State the blood parasite species.
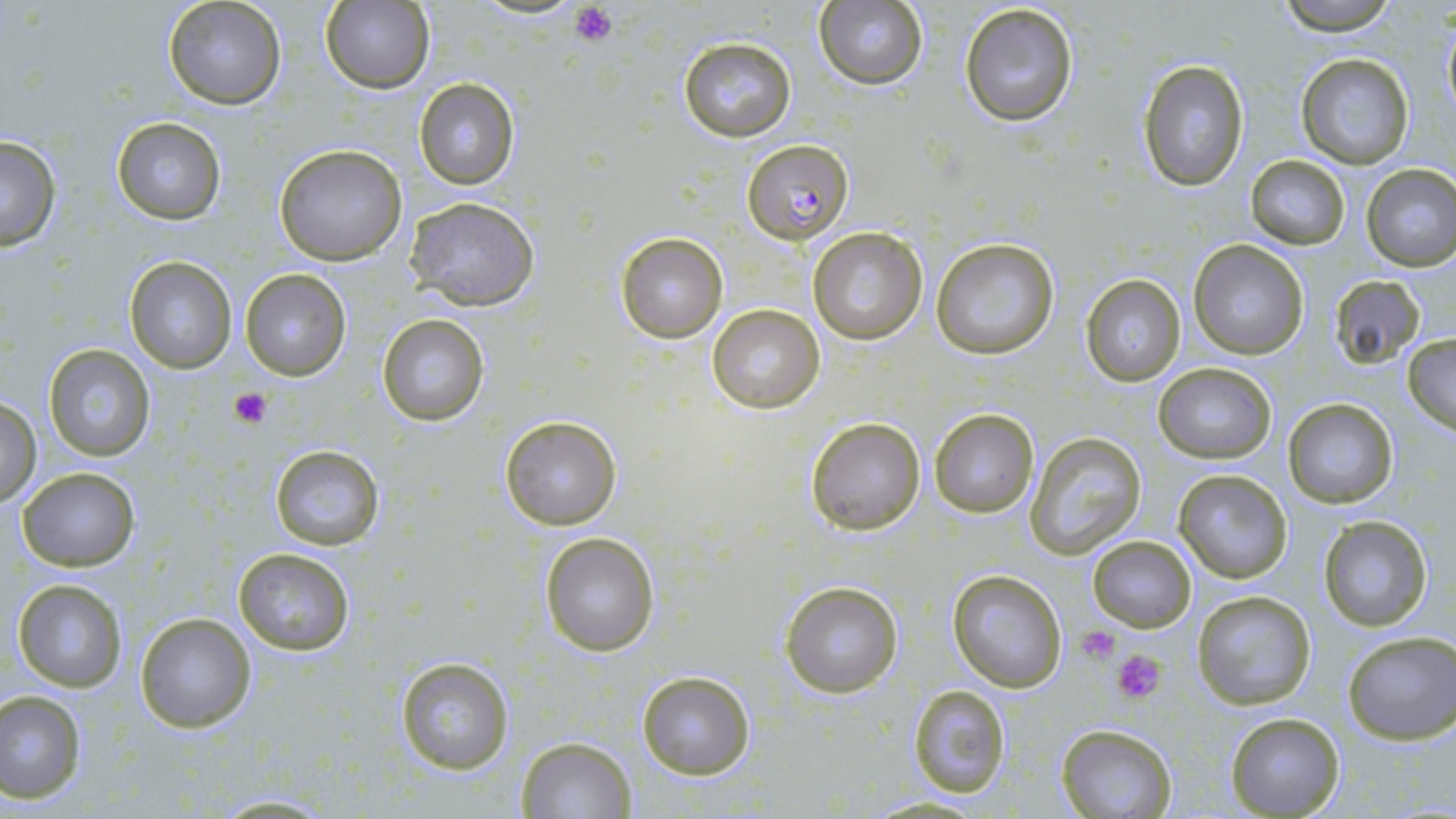

Plasmodium falciparum.

Summary:
  - Coordinate format: approximate bounding boxes as (x1, y1, x2, y2) in pixels
  - Plasmodium falciparum-infected red blood cell locations: (742, 140, 852, 242)
  - Uninfected red blood cell locations: (161, 0, 287, 111), (1273, 0, 1401, 33), (812, 1, 929, 90), (319, 2, 434, 92), (958, 2, 1079, 128), (1440, 9, 1456, 124), (676, 35, 797, 142), (1296, 53, 1413, 168), (1138, 58, 1249, 191), (414, 77, 519, 190), (110, 117, 227, 223), (0, 134, 63, 252), (272, 142, 407, 264), (1246, 154, 1349, 249), (1360, 163, 1456, 271), (404, 197, 542, 312), (807, 227, 929, 345), (615, 232, 728, 342), (929, 238, 1059, 359), (1188, 241, 1308, 360), (123, 255, 237, 372), (240, 268, 350, 381), (1330, 274, 1425, 368), (1081, 275, 1184, 386), (706, 304, 825, 415), (376, 314, 490, 426), (1401, 333, 1456, 432), (43, 343, 155, 461), (1155, 362, 1276, 463), (0, 396, 41, 506), (1282, 397, 1399, 509), (928, 408, 1040, 519), (500, 416, 621, 530), (806, 417, 927, 536), (1023, 431, 1148, 556), (268, 443, 384, 550), (16, 467, 140, 571), (1172, 469, 1292, 583), (1317, 515, 1435, 633), (540, 531, 661, 657), (1088, 535, 1195, 631), (232, 547, 357, 657), (948, 569, 1068, 692), (12, 577, 128, 693), (779, 578, 905, 700), (1191, 591, 1317, 712), (134, 611, 257, 733), (1342, 631, 1455, 745), (394, 656, 517, 775), (637, 671, 755, 779), (907, 684, 1012, 797), (0, 689, 86, 802), (1225, 710, 1344, 818), (1056, 724, 1177, 818), (515, 736, 636, 817)
  - Platelet locations: (570, 3, 617, 46), (229, 384, 273, 430), (1078, 626, 1121, 660), (1110, 647, 1169, 704)
  - Preparation: thin blood film
  - Modality: light microscopy
  - Field of view: one of a larger specimen
  - Image size: 1456×819 pixels
  - Stain: May-Grünwald-Giemsa
  - Magnification: 1000x